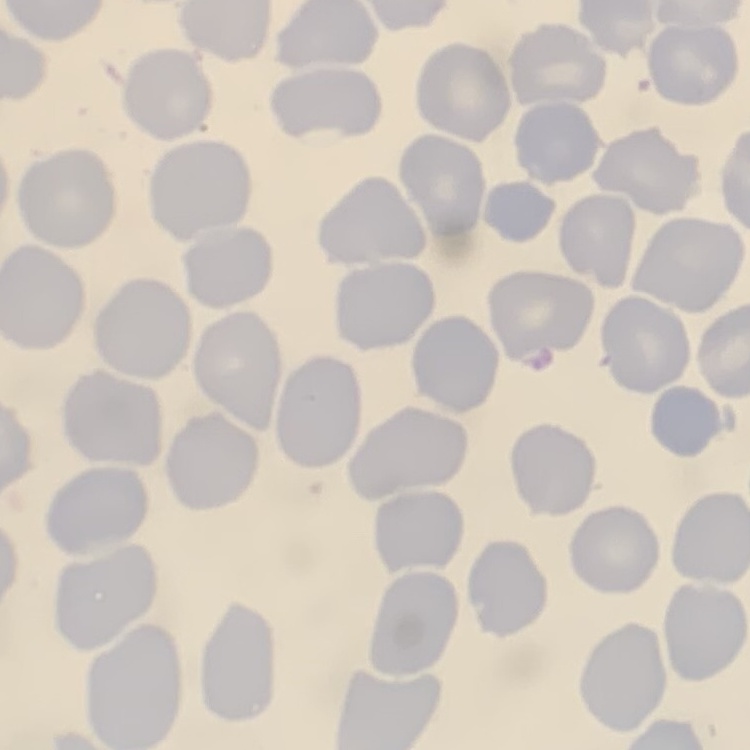
red blood cell morphology = no rouleaux formation
stain = Field's or Giemsa
preparation = thin blood film
image type = one tile cut from a larger photomicrograph